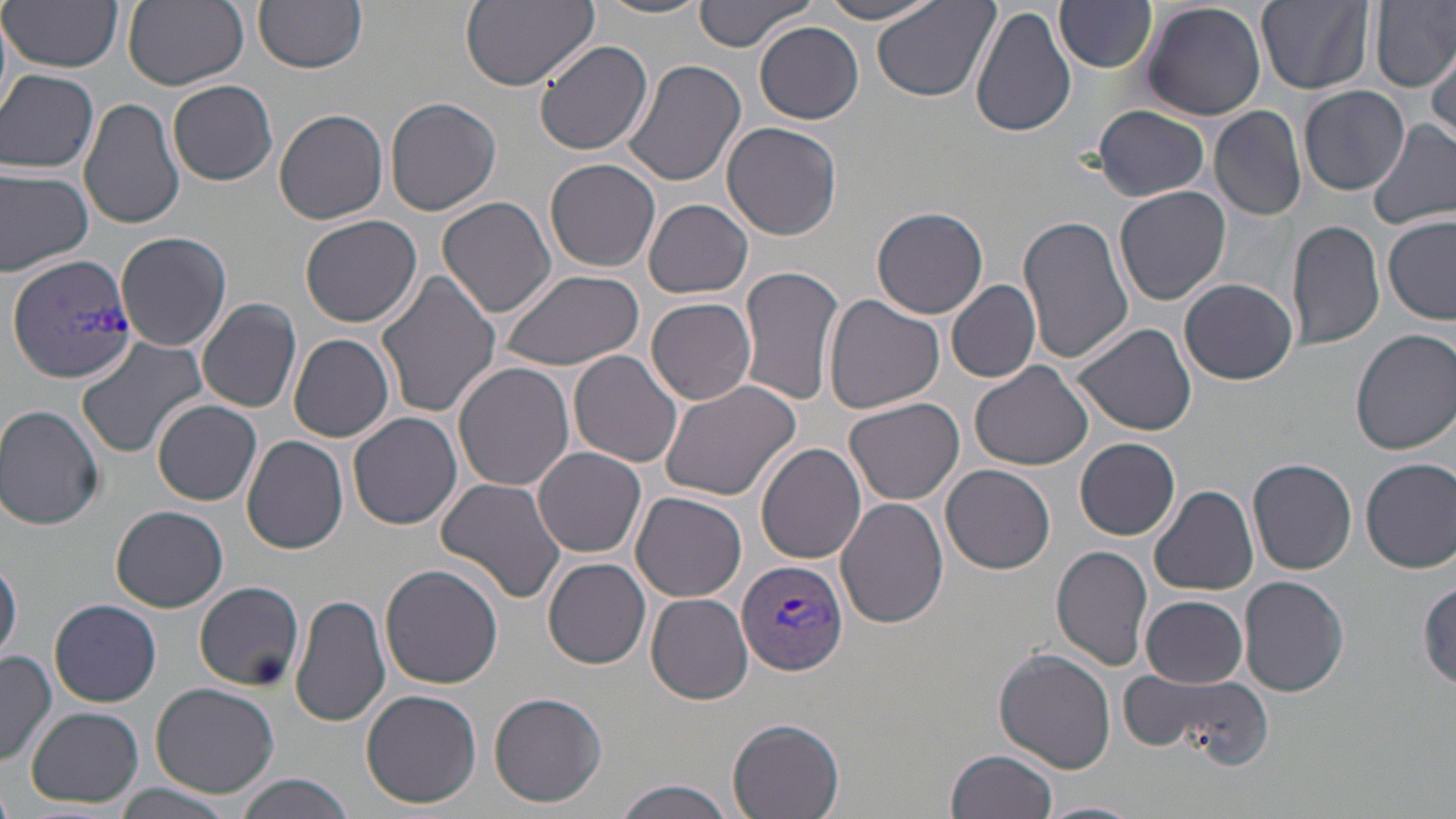

slide_level_diagnosis: Plasmodium vivax
field_of_view: single
stain: May-Grünwald-Giemsa
magnification: 1000x
plasmodium_vivax_infected_red_blood_cell_locations: 'approximate bounding boxes as [x1, y1, x2, y2] in pixels: [6, 254, 140, 386], [738, 559, 848, 675]'
uninfected_red_blood_cell_locations: 'approximate bounding boxes as [x1, y1, x2, y2] in pixels: [256, 0, 367, 73], [460, 0, 598, 90], [692, 0, 814, 51], [816, 0, 946, 24], [1054, 0, 1158, 74], [1257, 0, 1374, 94], [122, 1, 248, 88], [594, 1, 712, 21], [1140, 1, 1268, 122], [1371, 1, 1456, 92], [2, 2, 124, 72], [873, 2, 1000, 103], [970, 4, 1077, 139], [754, 20, 865, 124], [534, 38, 653, 156], [1427, 40, 1456, 149], [619, 58, 749, 189], [0, 68, 100, 173], [168, 78, 279, 185], [1299, 85, 1410, 197], [385, 98, 501, 217], [80, 99, 185, 228], [1092, 105, 1211, 203], [1209, 105, 1307, 222], [274, 109, 389, 224], [1368, 119, 1456, 232], [722, 122, 843, 242], [547, 159, 661, 273], [0, 168, 95, 275], [1114, 185, 1230, 308], [437, 196, 558, 319], [645, 200, 754, 299], [871, 208, 988, 319], [299, 214, 421, 328], [1018, 214, 1134, 366], [1382, 217, 1455, 324], [1288, 219, 1385, 351], [115, 230, 232, 353], [737, 267, 843, 407], [377, 270, 501, 420], [498, 270, 645, 374], [1178, 277, 1297, 385], [946, 278, 1042, 383], [824, 295, 944, 417], [197, 297, 302, 412], [646, 298, 757, 405], [1072, 321, 1200, 438], [1350, 328, 1456, 455], [289, 332, 394, 442], [76, 335, 208, 458], [570, 351, 683, 469], [453, 360, 576, 493], [968, 360, 1095, 470], [660, 376, 805, 502], [845, 397, 965, 506], [154, 400, 262, 506], [0, 404, 105, 530], [348, 412, 462, 530], [241, 435, 349, 553], [1075, 439, 1182, 541], [756, 444, 866, 566], [534, 447, 647, 560], [1360, 457, 1456, 573], [1247, 458, 1357, 575], [941, 465, 1056, 574], [435, 478, 566, 607], [1150, 485, 1258, 597], [630, 493, 747, 602], [838, 496, 950, 629], [111, 505, 228, 612], [1051, 545, 1154, 671], [1, 558, 23, 664], [544, 558, 651, 669], [380, 563, 504, 689], [1239, 576, 1349, 696], [193, 581, 304, 691], [1418, 583, 1455, 690], [291, 593, 391, 727], [646, 593, 753, 705], [1141, 594, 1248, 686], [50, 598, 161, 707], [994, 650, 1118, 774], [0, 651, 56, 767], [1120, 665, 1272, 765], [149, 681, 280, 799], [360, 689, 483, 808], [488, 691, 608, 808], [26, 707, 143, 807], [728, 717, 846, 819], [948, 749, 1059, 819], [235, 773, 355, 819], [614, 778, 736, 819], [112, 783, 240, 819], [1033, 801, 1141, 819]'
image_size: 1456×819 pixels
modality: optical microscopy
preparation: thin blood smear